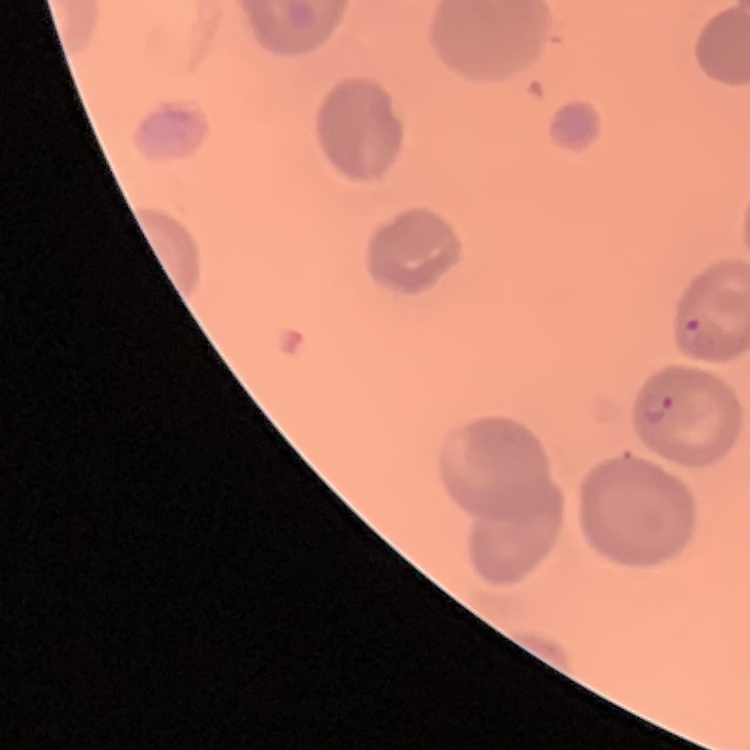

erythrocyte morphology = no rouleaux formation
preparation = thin blood film
image type = one tile cut from a larger photomicrograph
stain = Field's or Giemsa